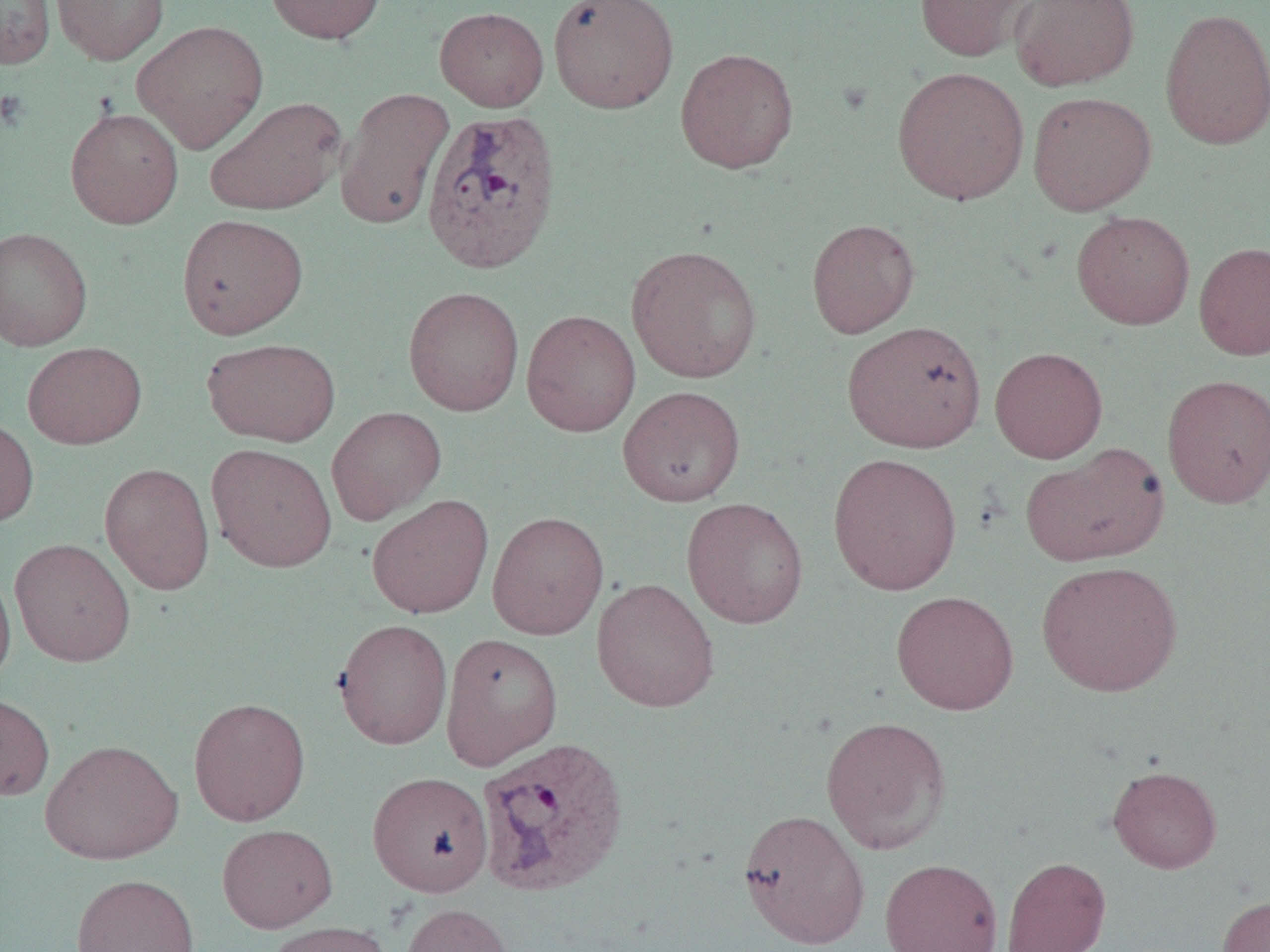

Approximate bounding boxes as named x1/y1/x2/y2 corners in pixels. Platelet locations: (x1=0, y1=89, x2=29, y2=130). Uninfected red blood cell locations: (x1=51, y1=0, x2=169, y2=65), (x1=264, y1=0, x2=386, y2=44), (x1=548, y1=0, x2=679, y2=113), (x1=914, y1=0, x2=1035, y2=61), (x1=1010, y1=0, x2=1140, y2=91), (x1=0, y1=1, x2=56, y2=68), (x1=435, y1=6, x2=549, y2=112), (x1=1159, y1=7, x2=1270, y2=151), (x1=132, y1=20, x2=270, y2=154), (x1=675, y1=48, x2=799, y2=173), (x1=891, y1=66, x2=1030, y2=205), (x1=335, y1=87, x2=454, y2=230), (x1=1027, y1=91, x2=1157, y2=216), (x1=204, y1=96, x2=347, y2=216), (x1=64, y1=107, x2=184, y2=229), (x1=1072, y1=211, x2=1195, y2=330), (x1=176, y1=213, x2=309, y2=339), (x1=806, y1=218, x2=920, y2=338), (x1=0, y1=227, x2=92, y2=350), (x1=1194, y1=241, x2=1270, y2=361), (x1=626, y1=244, x2=762, y2=383), (x1=403, y1=286, x2=524, y2=416), (x1=521, y1=309, x2=641, y2=437), (x1=842, y1=320, x2=987, y2=453), (x1=202, y1=337, x2=341, y2=446), (x1=23, y1=341, x2=147, y2=449), (x1=989, y1=346, x2=1108, y2=463), (x1=1161, y1=374, x2=1270, y2=508), (x1=617, y1=386, x2=745, y2=507), (x1=326, y1=406, x2=446, y2=524), (x1=0, y1=415, x2=38, y2=528), (x1=205, y1=443, x2=337, y2=572), (x1=1021, y1=443, x2=1169, y2=567), (x1=828, y1=452, x2=963, y2=595), (x1=99, y1=462, x2=215, y2=595), (x1=366, y1=494, x2=494, y2=619), (x1=681, y1=497, x2=809, y2=629), (x1=487, y1=511, x2=609, y2=640), (x1=10, y1=538, x2=136, y2=667), (x1=1036, y1=560, x2=1182, y2=697), (x1=0, y1=562, x2=16, y2=688), (x1=591, y1=578, x2=720, y2=713), (x1=891, y1=590, x2=1019, y2=715), (x1=333, y1=618, x2=453, y2=750), (x1=440, y1=633, x2=563, y2=770), (x1=0, y1=692, x2=55, y2=801), (x1=188, y1=697, x2=311, y2=826), (x1=821, y1=716, x2=952, y2=854), (x1=40, y1=738, x2=183, y2=865), (x1=1108, y1=765, x2=1222, y2=873), (x1=367, y1=771, x2=494, y2=897), (x1=738, y1=809, x2=871, y2=948), (x1=217, y1=823, x2=338, y2=933), (x1=1001, y1=856, x2=1111, y2=952), (x1=880, y1=858, x2=1003, y2=952), (x1=70, y1=873, x2=201, y2=952), (x1=1216, y1=894, x2=1270, y2=952), (x1=400, y1=903, x2=514, y2=952), (x1=264, y1=920, x2=393, y2=952). Plasmodium vivax-infected red blood cell locations: (x1=421, y1=108, x2=563, y2=275), (x1=465, y1=736, x2=618, y2=896). Slide-level diagnosis: Plasmodium vivax. Image is 1270×952 pixels. Captured at 1000x magnification. Single field of view. Thin blood film. Optical microscopy.